Describe the morphology of the red blood cells.
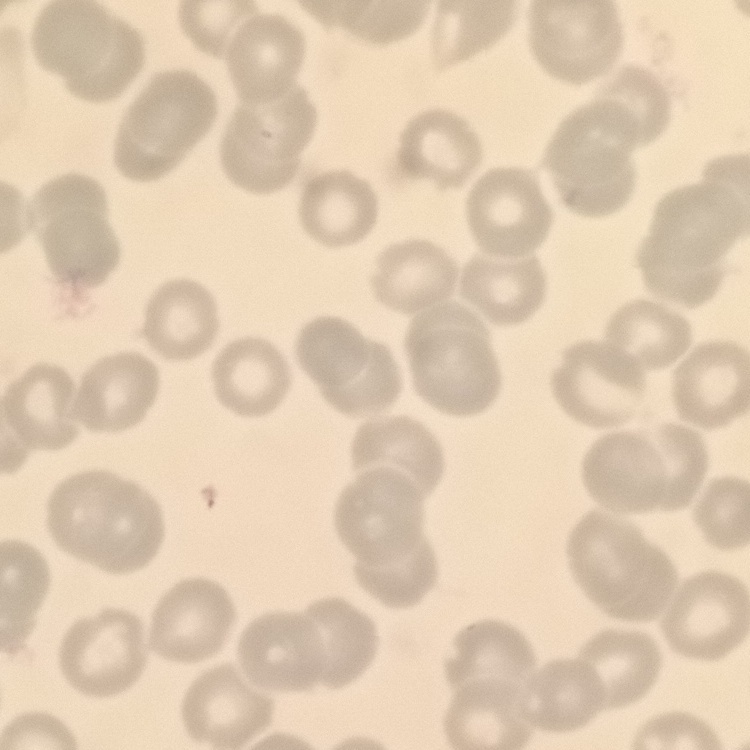
They show no rouleaux formation.

Square crop of a larger photomicrograph. Field's or Giemsa stain. Thin peripheral smear.